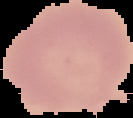

Summary:
  - Image size: 133×118 pixels
  - Preparation: thin blood film
  - Image type: segmented cell region with the area outside set to black
  - Result: no malaria parasites detected